Classify this cell by malaria status.
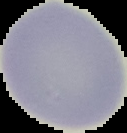
Uninfected.

image type = segmented cell region with the area outside set to black
preparation = thin blood smear
image size = 127×133 pixels